State which parasite is depicted.
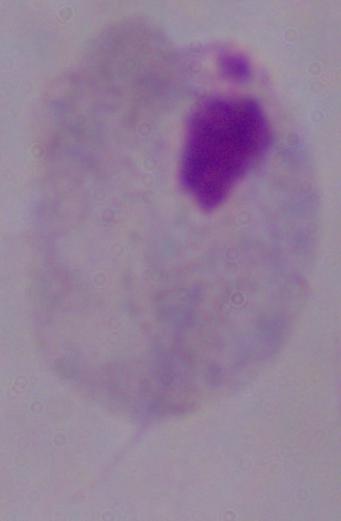

A trichomonad.

Summary:
  - Modality: micrograph
  - Magnification: 1000x